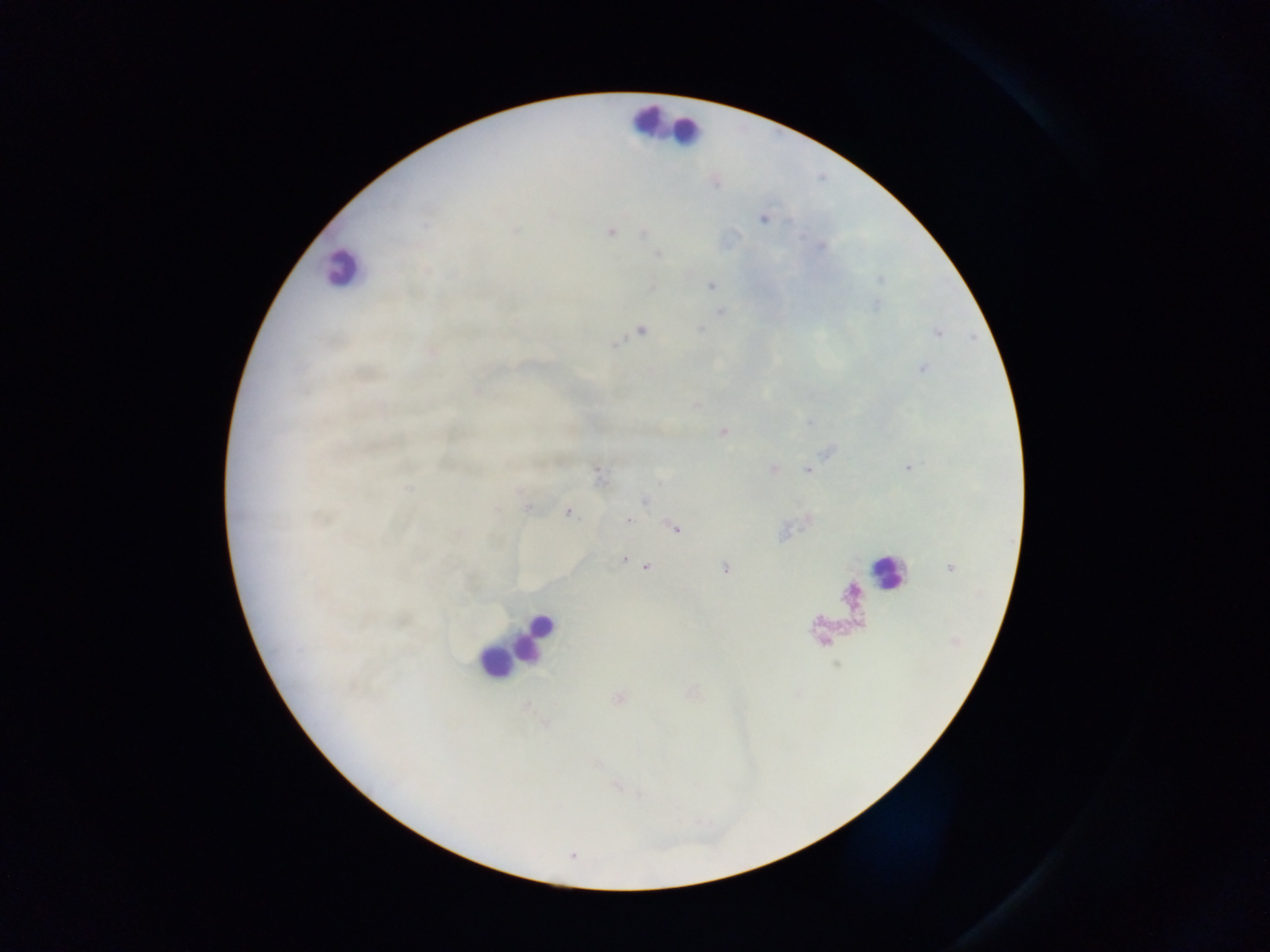
field of view = single
preparation = thick blood film
capture = mobile-phone photograph through a microscope
image size = 1270×952 pixels
leukocyte locations = approximate centers as (x, y) in pixels: (643, 122), (685, 131), (339, 270), (886, 574), (534, 639), (495, 665)
country = Ghana
Plasmodium parasite locations = approximate centers as (x, y) in pixels: (763, 218), (612, 231), (710, 286), (720, 312), (641, 330), (700, 330), (616, 344), (597, 473), (644, 500), (567, 513), (629, 520), (674, 529), (624, 559), (646, 567), (725, 569)